Give the position of every Plasmodium parasite visible.
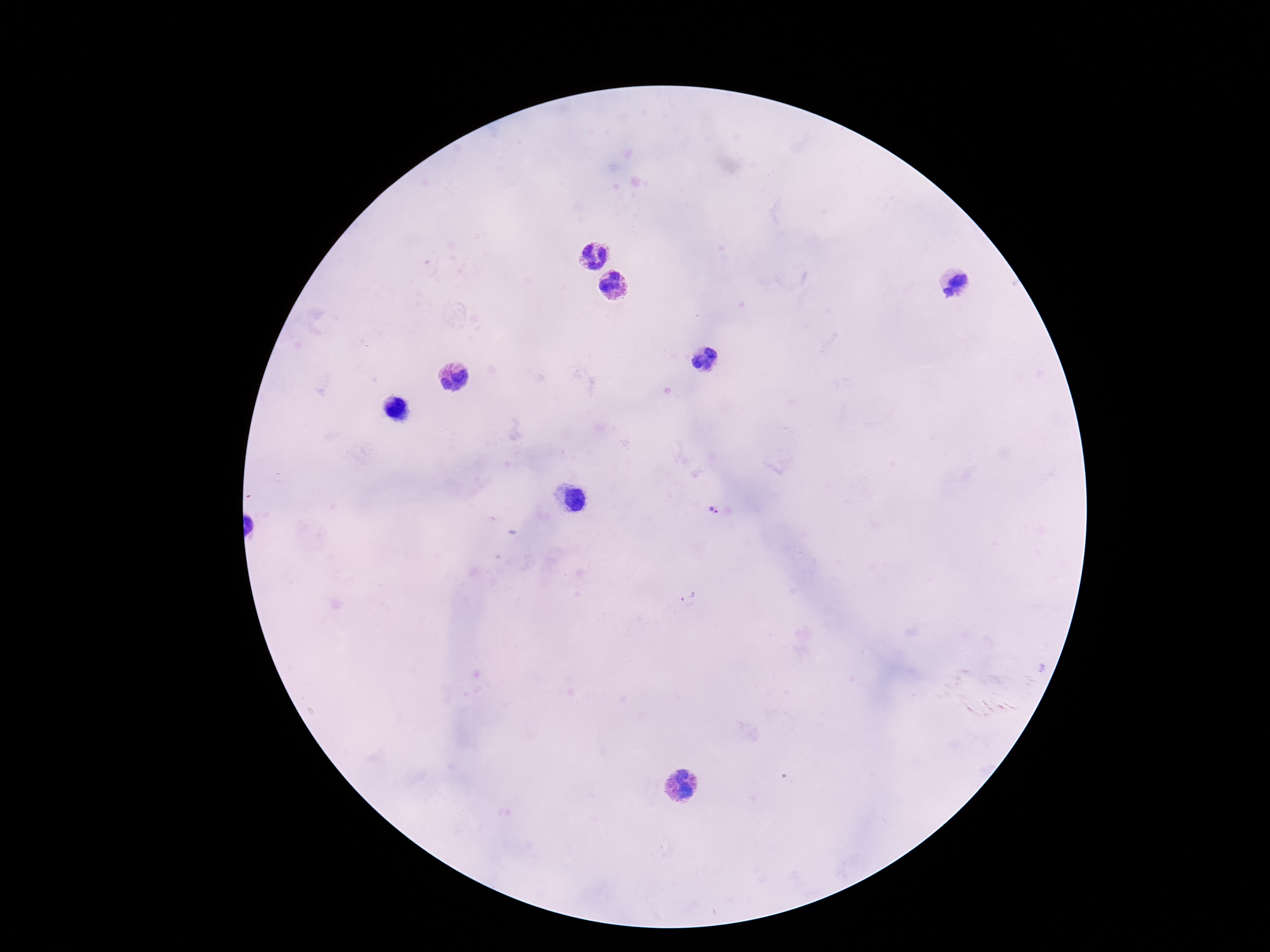
Approximate centers as [x, y] in pixels.
Plasmodium parasites: [713, 510], [689, 599].

field of view = one from this slide
stain = Giemsa
capture = smartphone camera through the microscope eyepiece
preparation = thick blood smear
patient malaria status = positive
image size = 1270×952 pixels
magnification = 100x